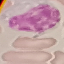
malaria status = uninfected
preparation = thin blood smear
stain = Giemsa
image type = automatically extracted cell patch, resized to 64 × 64 pixels
capture = smartphone through the microscope eyepiece